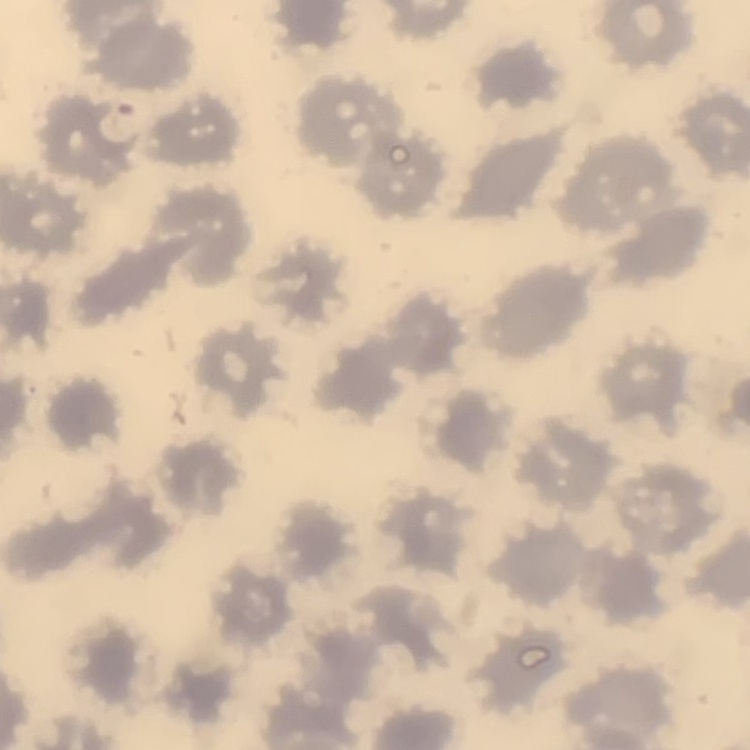

red blood cell morphology = no rouleaux formation
image type = square crop of a larger photomicrograph
stain = Field's or Giemsa
preparation = thin blood film